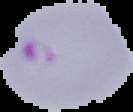

From a thin blood film. The area outside the segmented cell region is set to black. Image is 133×112 pixels. Malaria status: parasitized.